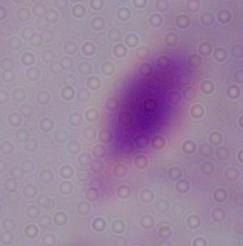

1000x magnification. Micrograph. A trichomonad is seen.